Name the cell type shown.
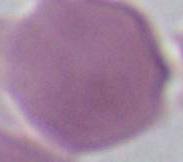

An erythrocyte.

Summary:
  - Magnification: 1000x
  - Modality: photomicrograph